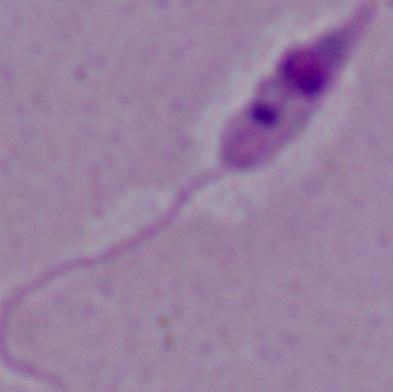

1000x magnification. A Leishmania parasite is seen. Photomicrograph.